Give the position of every malaria parasite.
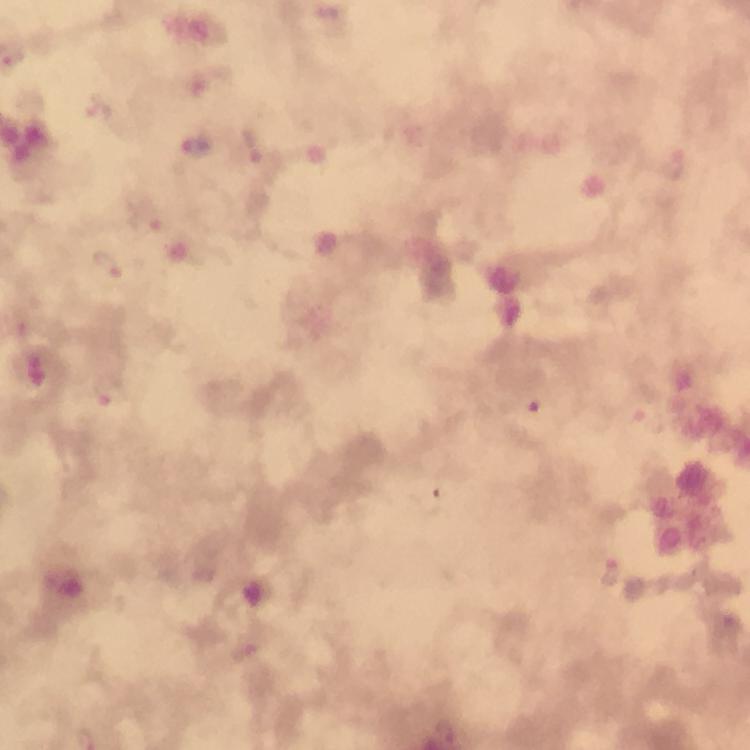

Approximate centers as {x, y} in pixels.
Malaria parasites: {100, 111}, {196, 148}, {256, 149}, {149, 218}, {111, 267}, {109, 390}, {611, 570}.

immersion oil = used
magnification = 100x
preparation = thick smear
cropped from = one field of view
capture = smartphone camera through the microscope
context = from a diagnostic examination for malaria
stain = Giemsa
image size = 750×750 pixels